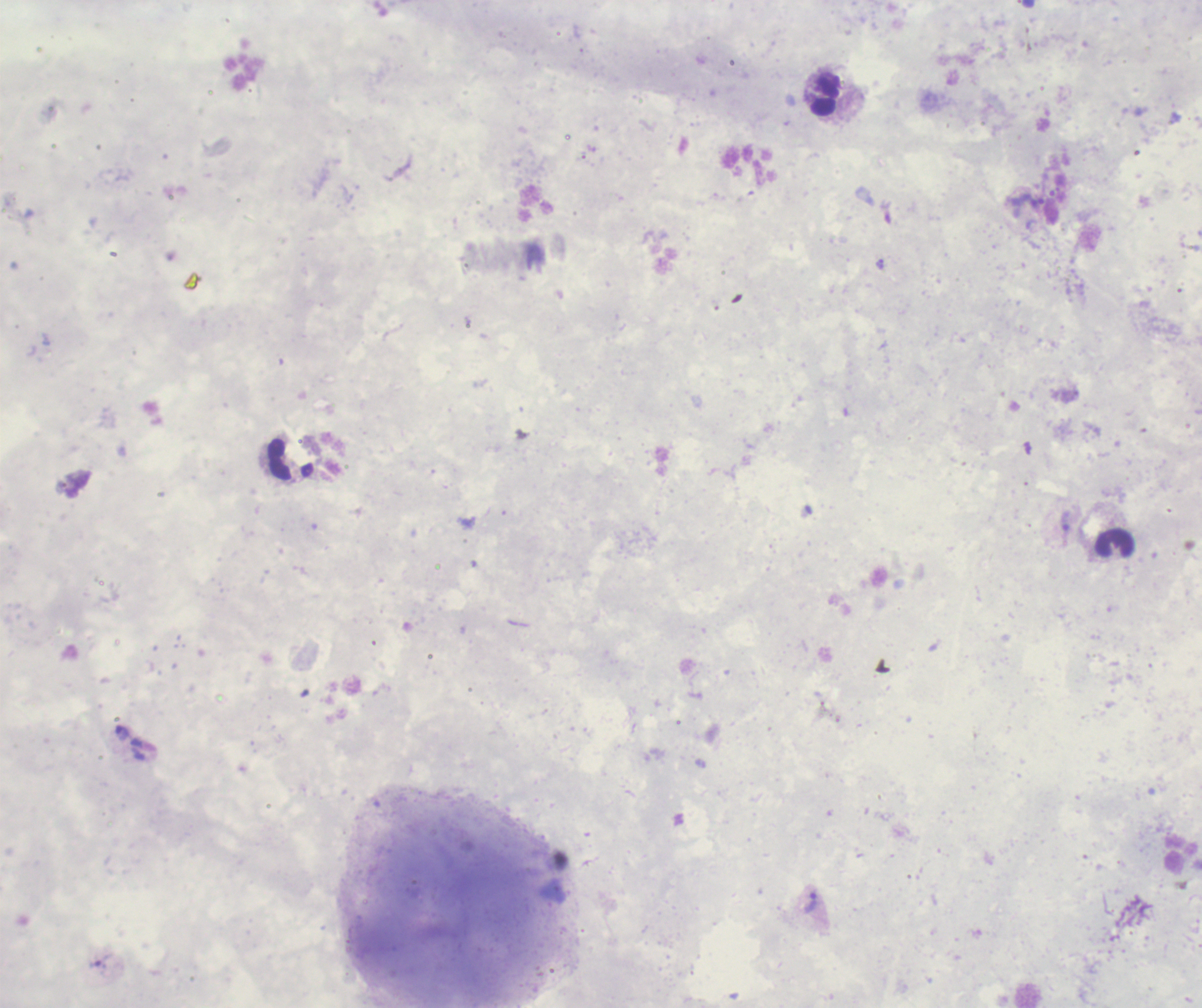

Approximate centers as [x, y] in pixels. Leukocyte locations: [826, 96], [1115, 542]. Trophozoite locations: [1032, 201], [123, 733], [812, 904]. Result: Plasmodium parasites detected. Previously used in a real diagnosis. Thick blood smear. Image is 1202×1008 pixels. Romanowsky-stained preparation. Background quality: poor. Captured at 100x magnification. Single field of view.